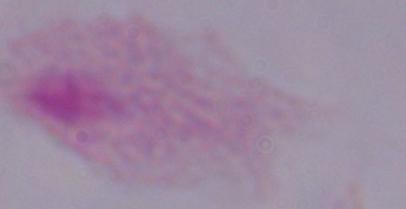

modality: micrograph
identification: trichomonad
magnification: 1000x